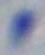

Summary:
  - Modality: micrograph
  - Identification: Toxoplasma gondii
  - Magnification: 1000x